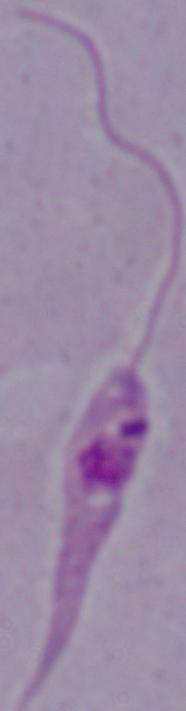
{
  "modality": "micrograph",
  "identification": "Leishmania",
  "magnification": "1000x"
}